Assess this cell for malaria.
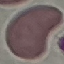
Uninfected.

image type = cell patch, automatically extracted from a larger field of view and resized to 64 × 64 pixels
capture = smartphone through the microscope eyepiece
preparation = thin blood smear
stain = Giemsa